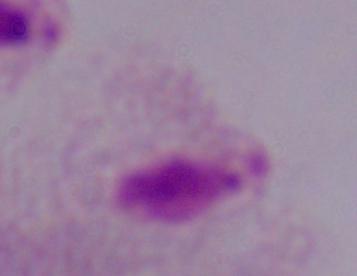
Summary:
  - Identification: trichomonad
  - Modality: micrograph
  - Magnification: 1000x